Give the position of every Plasmodium parasite and every leukocyte.
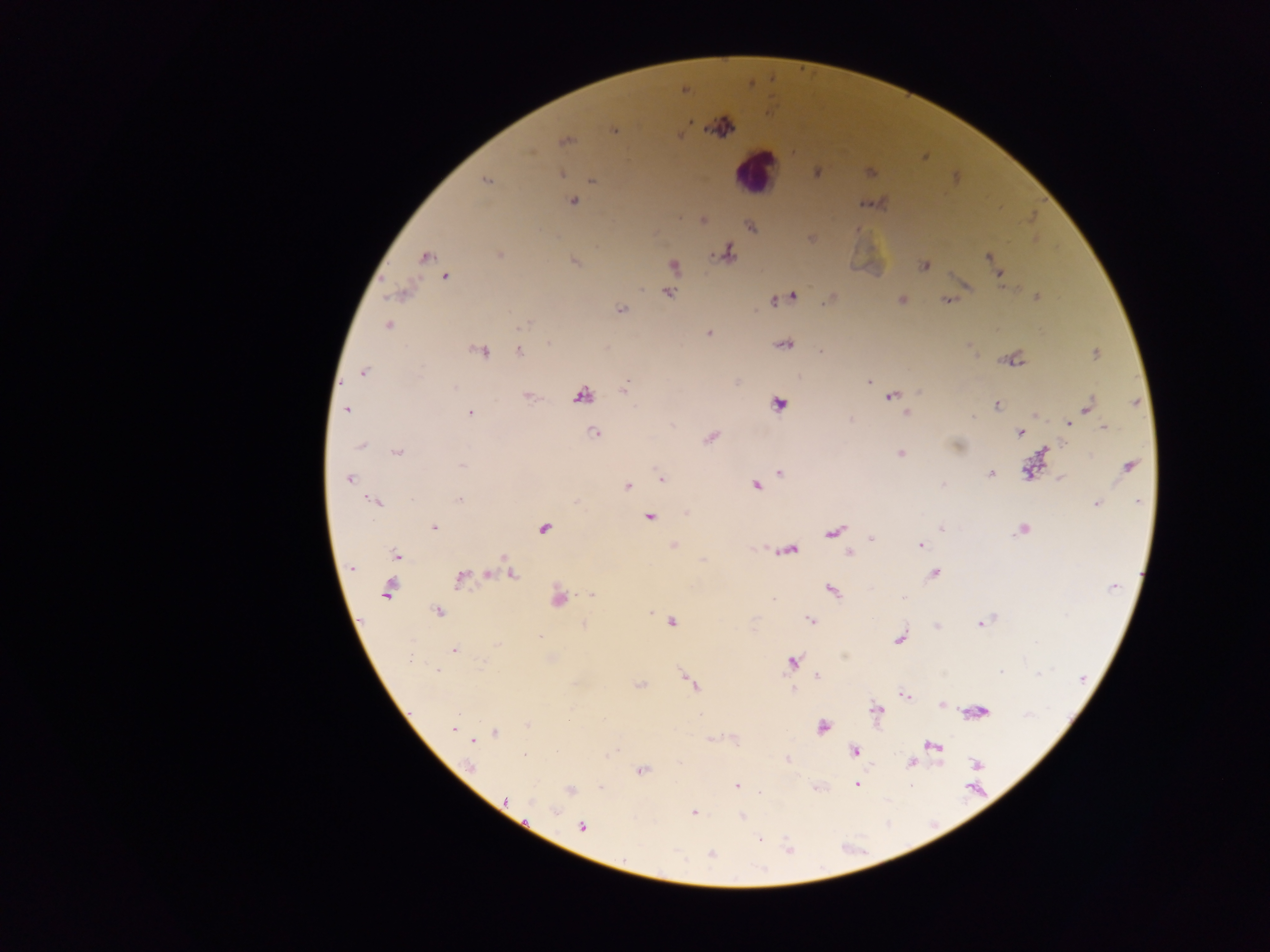

Approximate centers as [x, y] in pixels.
Plasmodium parasites: [721, 126], [563, 140], [531, 153], [816, 172], [561, 174], [486, 180], [592, 180], [575, 201], [1033, 215], [703, 218], [727, 251], [424, 257], [989, 258], [574, 261], [673, 266], [924, 266], [444, 277], [669, 291], [795, 295], [1037, 296], [945, 298], [901, 299], [772, 300], [620, 308], [523, 325], [387, 327], [709, 332], [784, 343], [548, 345], [820, 350], [482, 351], [519, 353], [1094, 354], [364, 372], [867, 381], [626, 383], [527, 395], [582, 395], [891, 396], [778, 402], [996, 404], [1087, 406], [346, 409], [471, 412], [907, 412], [972, 415], [1067, 424], [1103, 425], [594, 433], [1020, 433], [710, 437], [956, 446], [360, 447], [1045, 449], [398, 452], [899, 453], [463, 466], [1128, 466], [781, 471], [990, 472], [1028, 472], [661, 478], [1061, 478], [350, 479], [944, 484], [627, 485], [757, 486], [460, 500], [371, 501], [1137, 502], [1096, 503], [687, 513], [649, 517], [941, 528], [1022, 528], [434, 529], [544, 529], [834, 532], [872, 539], [920, 544], [674, 545], [793, 551], [850, 552], [398, 557], [503, 558], [350, 567], [933, 573], [513, 576], [461, 580], [386, 588], [832, 591], [591, 595], [903, 598], [559, 599], [774, 599], [437, 611], [650, 613], [811, 621], [671, 622], [583, 624], [978, 624], [541, 637], [898, 640], [496, 644], [455, 648], [844, 657], [409, 659], [793, 661], [482, 662], [438, 671], [1002, 672], [1036, 676], [684, 677], [817, 677], [690, 683], [641, 687], [792, 691], [941, 705], [878, 708], [527, 726], [822, 726], [453, 728], [495, 732], [710, 739], [472, 741], [931, 745], [938, 748], [853, 751], [613, 753], [608, 754], [525, 757], [788, 758], [911, 763], [937, 764], [976, 765], [641, 771], [857, 783], [736, 787], [599, 789], [570, 790], [759, 791], [505, 800], [555, 810], [693, 813], [741, 816], [581, 826], [758, 839], [789, 847], [710, 854].
Leukocytes: [760, 165].

preparation = thick blood film
capture = mobile-phone photograph through a microscope
image size = 1270×952 pixels
field of view = single
country = Ghana